Outline each white blood cell.
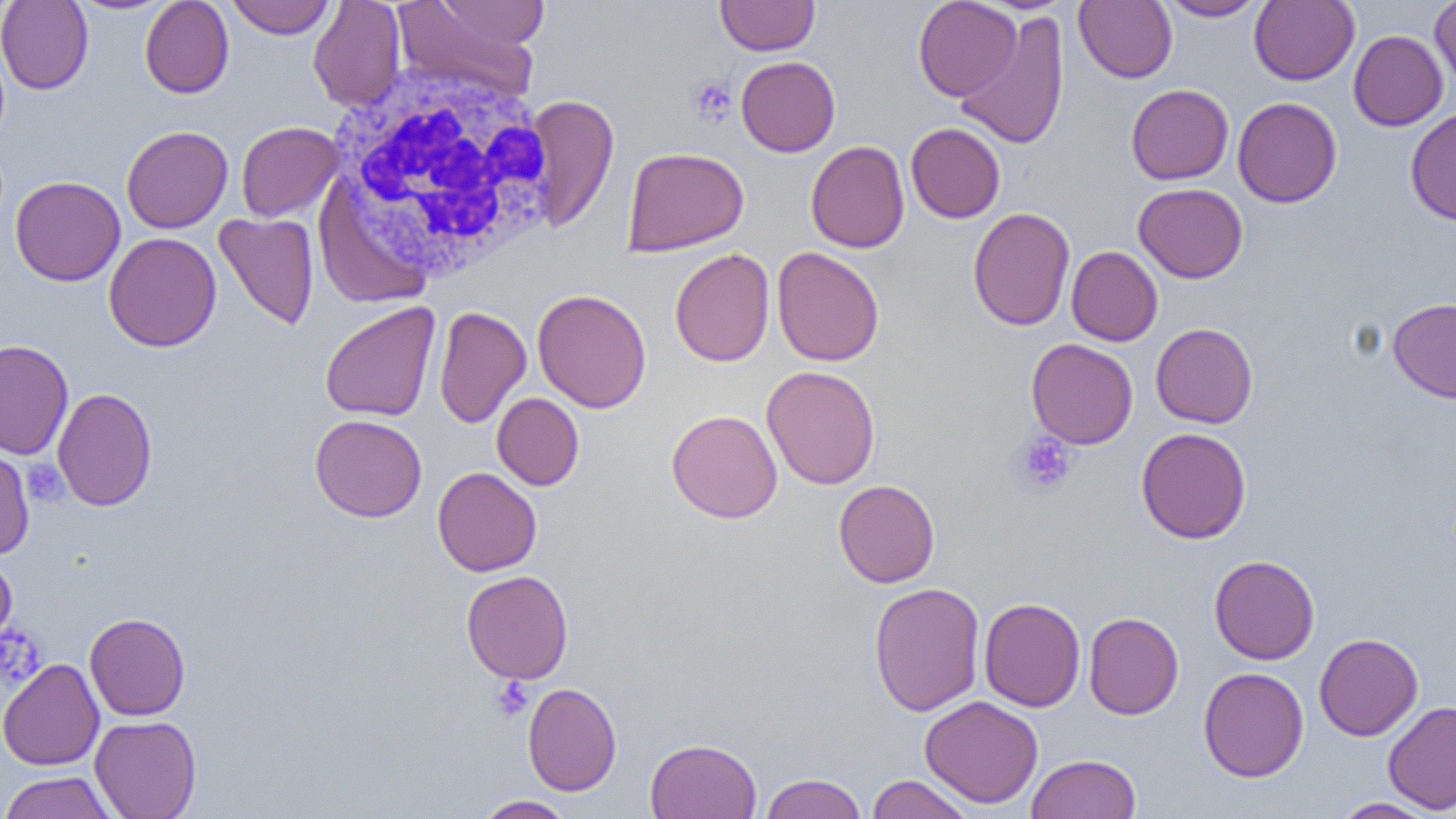

Approximate bounding boxes as named x1/y1/x2/y2 corners in pixels.
White blood cells: (x1=327, y1=60, x2=561, y2=282).

Platelet locations: (x1=686, y1=76, x2=737, y2=126), (x1=1010, y1=432, x2=1078, y2=497), (x1=23, y1=459, x2=67, y2=505), (x1=0, y1=625, x2=46, y2=692), (x1=490, y1=676, x2=534, y2=721). Uninfected red blood cell locations: (x1=0, y1=0, x2=93, y2=94), (x1=67, y1=0, x2=178, y2=15), (x1=140, y1=0, x2=234, y2=98), (x1=226, y1=0, x2=335, y2=39), (x1=437, y1=0, x2=549, y2=50), (x1=715, y1=0, x2=819, y2=56), (x1=912, y1=0, x2=1022, y2=101), (x1=1157, y1=0, x2=1267, y2=21), (x1=1249, y1=0, x2=1360, y2=86), (x1=1430, y1=0, x2=1456, y2=93), (x1=308, y1=1, x2=406, y2=112), (x1=391, y1=1, x2=541, y2=101), (x1=1073, y1=1, x2=1177, y2=83), (x1=954, y1=10, x2=1070, y2=151), (x1=1348, y1=30, x2=1448, y2=131), (x1=736, y1=56, x2=840, y2=156), (x1=1126, y1=84, x2=1234, y2=184), (x1=524, y1=95, x2=619, y2=232), (x1=1233, y1=97, x2=1342, y2=207), (x1=1405, y1=107, x2=1456, y2=226), (x1=236, y1=121, x2=343, y2=222), (x1=905, y1=123, x2=1006, y2=223), (x1=121, y1=125, x2=233, y2=234), (x1=805, y1=140, x2=909, y2=253), (x1=622, y1=147, x2=749, y2=256), (x1=10, y1=176, x2=125, y2=286), (x1=1133, y1=182, x2=1248, y2=283), (x1=967, y1=207, x2=1075, y2=331), (x1=214, y1=212, x2=319, y2=331), (x1=103, y1=232, x2=222, y2=352), (x1=1066, y1=246, x2=1163, y2=346), (x1=771, y1=247, x2=885, y2=367), (x1=670, y1=248, x2=774, y2=367), (x1=532, y1=288, x2=651, y2=413), (x1=1387, y1=297, x2=1456, y2=403), (x1=319, y1=301, x2=441, y2=422), (x1=433, y1=305, x2=531, y2=428), (x1=1150, y1=323, x2=1258, y2=428), (x1=1025, y1=338, x2=1138, y2=449), (x1=0, y1=339, x2=74, y2=460), (x1=761, y1=365, x2=881, y2=489), (x1=52, y1=387, x2=157, y2=511), (x1=492, y1=392, x2=584, y2=490), (x1=666, y1=409, x2=783, y2=523), (x1=309, y1=414, x2=427, y2=523), (x1=1135, y1=427, x2=1252, y2=544), (x1=0, y1=445, x2=35, y2=560), (x1=432, y1=467, x2=541, y2=577), (x1=833, y1=479, x2=940, y2=588), (x1=0, y1=553, x2=17, y2=653), (x1=1209, y1=554, x2=1320, y2=665), (x1=460, y1=570, x2=573, y2=684), (x1=868, y1=582, x2=985, y2=716), (x1=979, y1=597, x2=1085, y2=712), (x1=84, y1=612, x2=190, y2=720), (x1=1083, y1=612, x2=1184, y2=720), (x1=1314, y1=633, x2=1423, y2=740), (x1=0, y1=658, x2=104, y2=771), (x1=1198, y1=667, x2=1309, y2=782), (x1=522, y1=682, x2=622, y2=796), (x1=919, y1=695, x2=1043, y2=809), (x1=1383, y1=700, x2=1456, y2=814), (x1=89, y1=715, x2=202, y2=819), (x1=645, y1=738, x2=762, y2=818), (x1=1026, y1=753, x2=1141, y2=819), (x1=0, y1=770, x2=119, y2=819), (x1=760, y1=772, x2=867, y2=819), (x1=866, y1=774, x2=975, y2=819), (x1=474, y1=795, x2=576, y2=818), (x1=1332, y1=797, x2=1440, y2=818). Slide-level diagnosis: no evidence of blood parasites. Light microscopy. Thin blood film. One field of a larger specimen. Image is 1456×819 pixels. Captured at 1000x magnification.